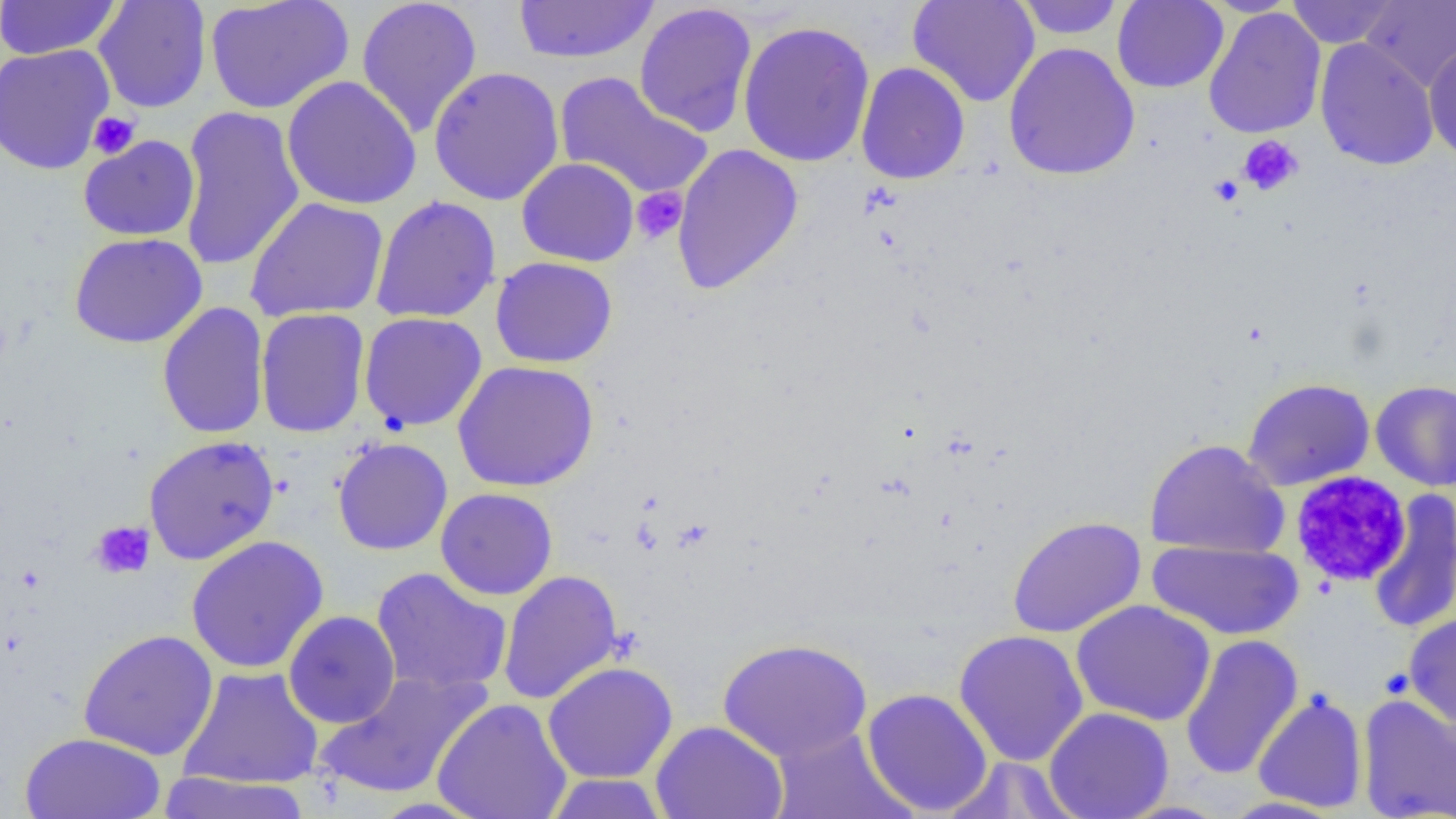
Approximate bounding boxes as (x1,y1)-(x2,y2) corner pairs in pixels. Platelet locations: (87,112)-(140,159), (1237,135)-(1303,196), (1209,175)-(1244,206), (631,187)-(688,245), (1289,470)-(1411,588), (90,521)-(155,579). Uninfected red blood cell locations: (0,0)-(123,60), (355,0)-(483,138), (907,0)-(1040,108), (1015,0)-(1126,40), (1112,0)-(1229,93), (1200,0)-(1304,16), (1286,0)-(1400,48), (93,1)-(212,113), (205,1)-(354,114), (513,1)-(660,64), (1360,1)-(1455,91), (633,3)-(758,137), (1204,7)-(1326,139), (737,20)-(876,168), (1315,38)-(1439,171), (1003,42)-(1140,181), (0,43)-(115,175), (1424,43)-(1456,164), (856,62)-(970,184), (428,67)-(565,206), (554,72)-(712,200), (281,75)-(422,211), (177,105)-(305,271), (79,135)-(200,241), (671,143)-(804,295), (517,158)-(639,267), (370,196)-(501,323), (245,197)-(388,322), (68,232)-(207,349), (490,256)-(618,368), (157,302)-(270,438), (256,307)-(370,438), (358,312)-(487,432), (452,360)-(599,492), (1242,378)-(1375,491), (1370,379)-(1456,491), (143,434)-(280,565), (332,437)-(453,555), (1144,438)-(1289,559), (435,487)-(558,600), (1368,489)-(1456,635), (1007,516)-(1146,638), (186,535)-(329,674), (1146,538)-(1305,641), (371,567)-(512,696), (498,569)-(624,705), (1071,600)-(1215,726), (283,610)-(400,728), (1404,613)-(1456,731), (78,629)-(219,761), (953,629)-(1089,767), (1180,634)-(1304,780), (717,637)-(873,762), (542,661)-(678,783), (176,666)-(324,791), (314,669)-(492,800), (861,687)-(994,816), (1252,691)-(1368,812), (1357,695)-(1456,819), (431,698)-(573,819), (1043,707)-(1174,819), (650,721)-(788,819), (768,726)-(915,819), (20,732)-(166,819), (940,758)-(1083,819), (156,771)-(314,819), (543,774)-(670,818), (1219,796)-(1345,818). Slide-level diagnosis: no evidence of blood parasites. Image is 1456×819 pixels. Single field of view. Light microscopy. 1000x magnification. Thin blood smear.